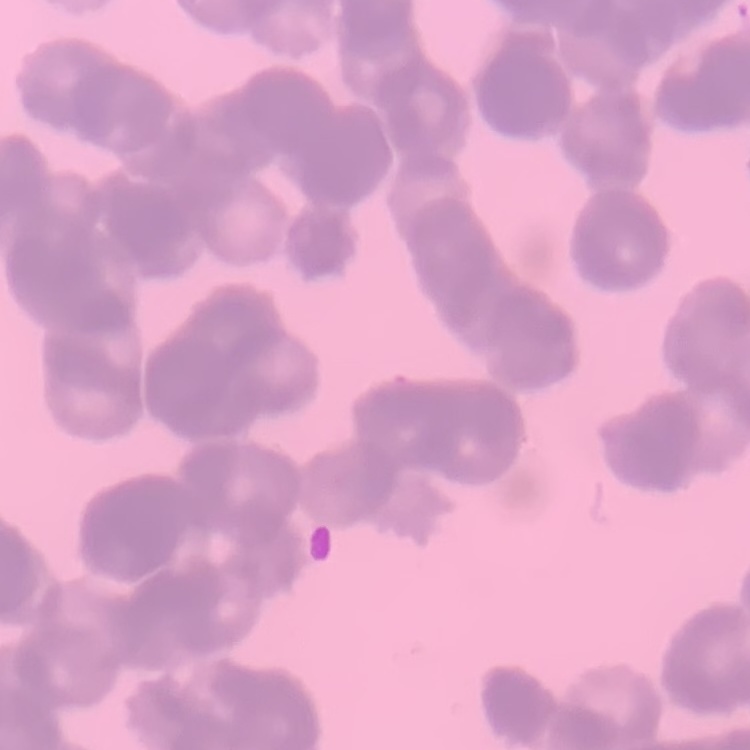
Summary:
  - Erythrocyte morphology: rouleaux formation
  - Stain: Field's or Giemsa
  - Preparation: thin blood film
  - Image type: one tile cut from a larger photomicrograph